Outline each blood parasite and name the species.
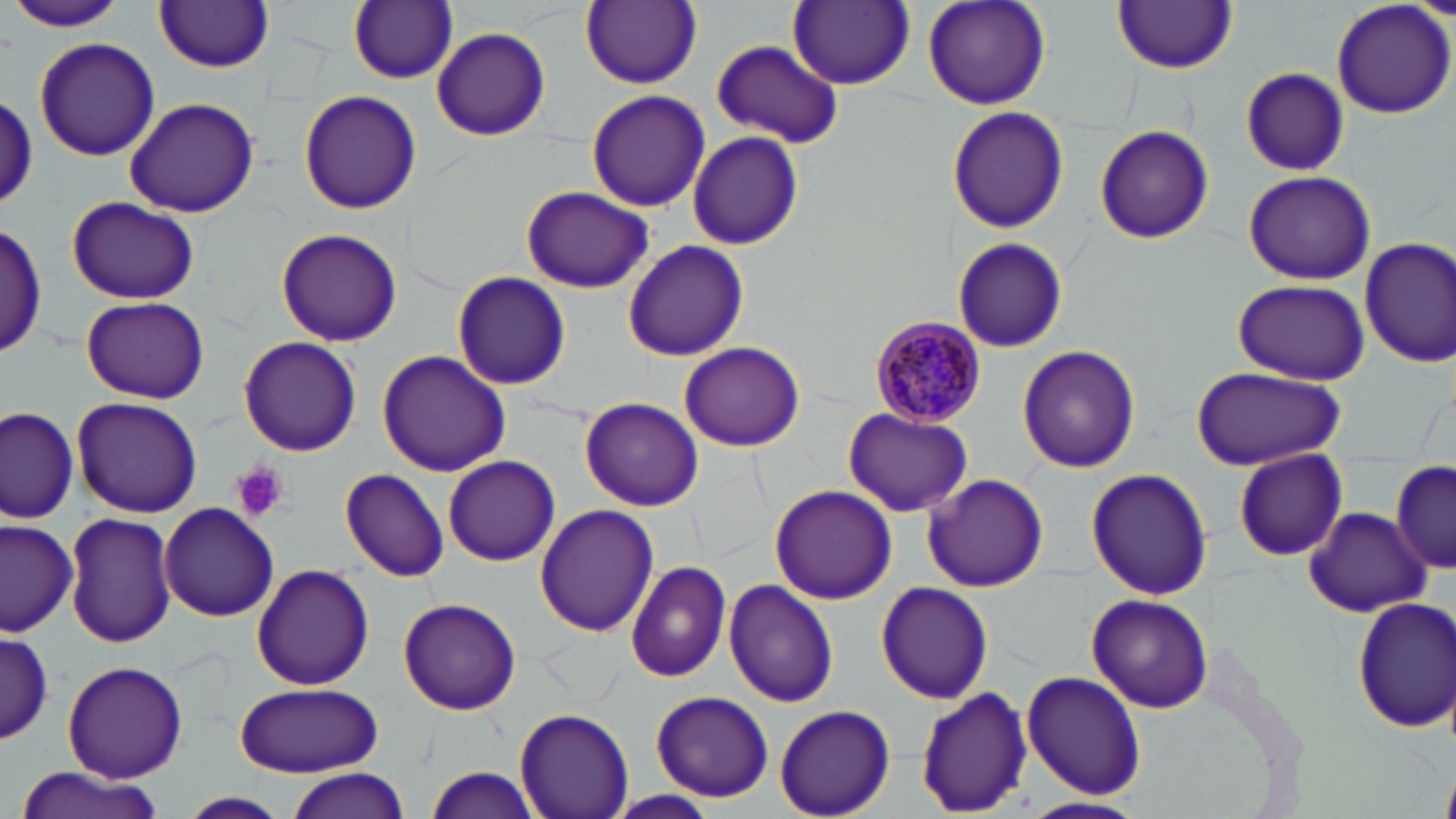
Approximate bounding boxes as (x1,y1)-(x2,y2) corner pairs in pixels.
Plasmodium malariae-infected red blood cells: (868,315)-(986,426).
No Plasmodium falciparum, Plasmodium ovale, Plasmodium vivax, Babesia divergens, or Trypanosoma brucei observed.

Summary:
  - Uninfected red blood cell locations: (921,0)-(1053,112), (1331,0)-(1456,119), (348,1)-(458,85), (581,1)-(701,89), (787,1)-(915,89), (1112,1)-(1238,73), (153,2)-(274,73), (8,3)-(130,34), (433,27)-(549,141), (33,36)-(159,162), (710,39)-(841,147), (1241,68)-(1348,175), (297,90)-(421,214), (584,90)-(709,212), (2,93)-(38,213), (123,96)-(260,218), (948,104)-(1068,233), (1095,123)-(1215,245), (687,132)-(803,249), (1241,171)-(1378,284), (520,186)-(656,295), (67,196)-(199,305), (1,222)-(47,359), (275,228)-(402,348), (952,236)-(1068,353), (1359,237)-(1456,368), (622,240)-(748,361), (451,271)-(572,391), (1231,279)-(1368,383), (80,295)-(209,404), (238,337)-(363,456), (680,341)-(805,452), (1018,346)-(1141,472), (377,350)-(512,476), (1190,365)-(1346,472), (71,396)-(203,518), (579,396)-(704,510), (1,406)-(79,523), (75,408)-(193,628), (843,408)-(973,517), (1233,449)-(1348,560), (443,455)-(560,566), (1391,461)-(1454,575), (1086,467)-(1212,601), (341,468)-(449,582), (922,472)-(1049,592), (769,484)-(898,604), (159,502)-(281,621), (534,503)-(658,636), (1302,506)-(1433,617), (64,512)-(178,649), (0,519)-(80,635), (625,560)-(732,683), (252,563)-(375,690), (724,579)-(839,707), (876,580)-(993,704), (1086,594)-(1213,714), (398,596)-(522,715), (1353,597)-(1456,732), (0,629)-(54,745), (63,661)-(187,782), (1021,671)-(1147,799), (234,682)-(385,778), (914,687)-(1031,814), (650,690)-(775,801), (774,704)-(895,819), (516,706)-(634,818), (8,766)-(168,819), (424,767)-(540,819), (280,768)-(410,819), (1442,769)-(1456,819), (609,791)-(721,816), (179,792)-(289,818), (1018,795)-(1146,819)
  - Platelet locations: (231,465)-(287,522)
  - Slide-level diagnosis: Plasmodium malariae
  - Stain: May-Grünwald-Giemsa
  - Preparation: thin blood smear
  - Magnification: 1000x
  - Field of view: single
  - Modality: optical microscopy
  - Image size: 1456×819 pixels